Report the malaria status of this cell.
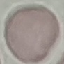
Uninfected.

Summary:
  - Image type: automatically extracted cell patch, resized to 64 × 64 pixels
  - Preparation: thin smear
  - Stain: Giemsa
  - Capture: smartphone camera at the microscope eyepiece